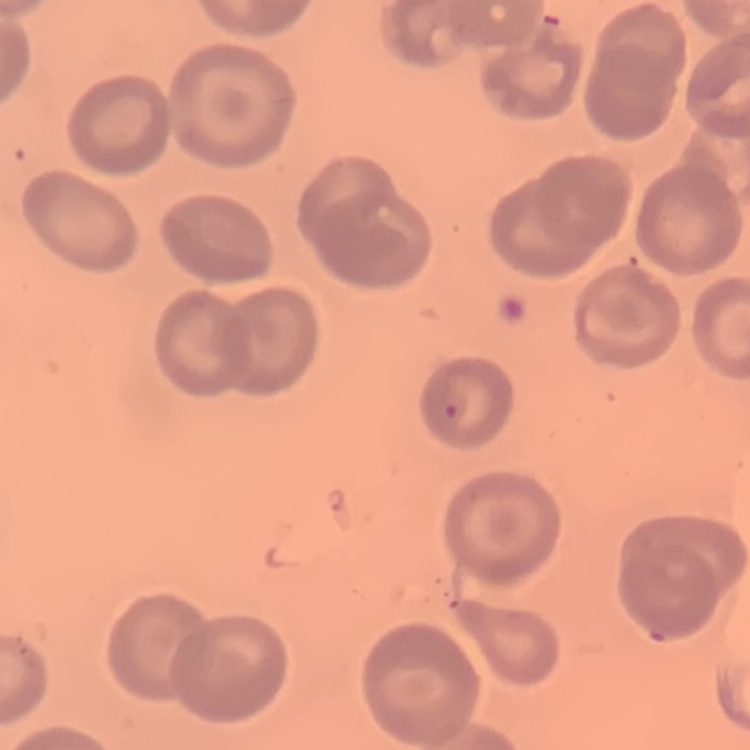 The red blood cells show no rouleaux formation. One tile cut from a larger photomicrograph. Thin blood film. Stained with either Field's or Giemsa.